Outline each blood parasite and name the species.
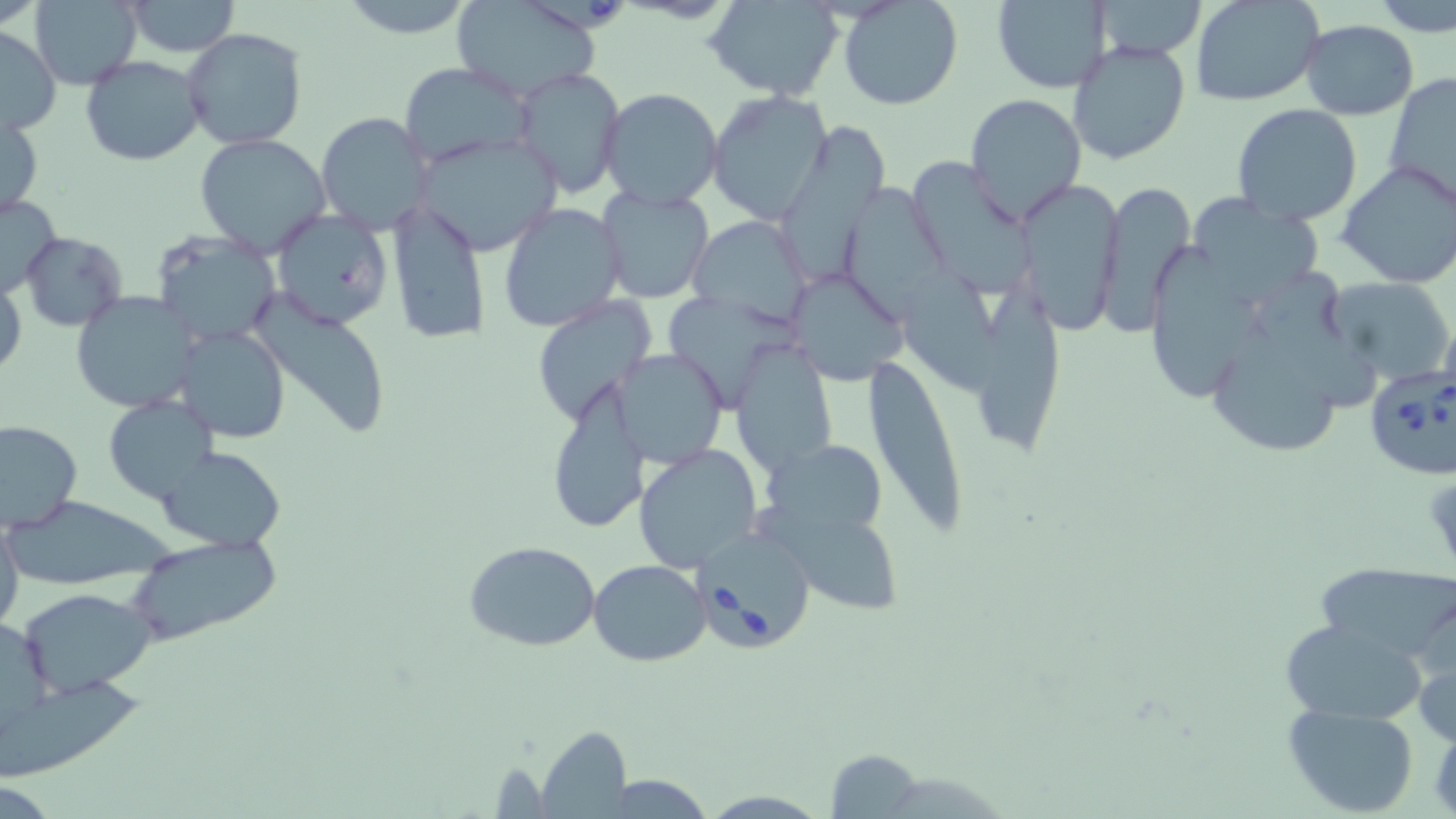
Approximate bounding boxes as (x1,y1)-(x2,y2) corner pairs in pixels.
Babesia divergens-infected red blood cells: (1364,361)-(1456,483), (690,527)-(818,653).
No Plasmodium falciparum, Plasmodium ovale, Plasmodium malariae, Plasmodium vivax, or Trypanosoma brucei observed.

Summary:
  - Uninfected red blood cell locations: (339,0)-(481,39), (837,0)-(963,111), (1092,0)-(1206,61), (1192,0)-(1324,106), (1372,0)-(1456,36), (30,1)-(143,87), (121,1)-(241,55), (452,1)-(604,100), (707,1)-(843,100), (991,1)-(1112,92), (1301,19)-(1419,119), (0,26)-(60,135), (182,27)-(307,150), (1068,40)-(1191,166), (80,55)-(205,166), (398,62)-(535,168), (513,67)-(624,197), (1384,72)-(1456,212), (599,87)-(723,209), (705,92)-(834,222), (965,93)-(1087,221), (1232,104)-(1363,228), (1,109)-(44,220), (316,111)-(434,236), (783,120)-(889,285), (194,133)-(331,256), (415,133)-(563,256), (902,155)-(1037,295), (1336,159)-(1456,289), (1014,176)-(1125,339), (1095,176)-(1196,334), (847,183)-(947,325), (596,186)-(715,305), (0,194)-(61,298), (1185,196)-(1325,305), (387,199)-(491,345), (499,202)-(628,331), (270,209)-(393,329), (690,215)-(815,328), (19,231)-(128,331), (150,232)-(284,346), (1140,237)-(1264,398), (904,257)-(1006,404), (786,271)-(908,383), (1261,271)-(1381,408), (1,273)-(25,381), (1324,275)-(1455,385), (971,276)-(1069,454), (69,292)-(197,412), (674,292)-(800,404), (248,293)-(394,439), (531,297)-(658,427), (1216,316)-(1343,460), (176,325)-(293,444), (735,336)-(836,482), (862,347)-(971,542), (608,349)-(731,468), (543,386)-(650,533), (104,396)-(220,506), (1,419)-(82,532), (764,442)-(895,538), (633,444)-(763,571), (160,447)-(285,550), (5,499)-(181,581), (754,505)-(909,615), (0,518)-(24,636), (121,534)-(284,647), (463,540)-(602,652), (589,560)-(710,666), (1313,561)-(1456,669), (18,586)-(157,698), (1276,618)-(1431,725), (1413,634)-(1456,750), (0,680)-(145,781), (1283,702)-(1420,817), (534,727)-(633,817), (824,748)-(925,819)
  - Slide-level diagnosis: Babesia divergens
  - Preparation: thin blood film
  - Magnification: 1000x
  - Image size: 1456×819 pixels
  - Field of view: single
  - Stain: May-Grünwald-Giemsa
  - Modality: light microscopy